Locate and identify every blood parasite.
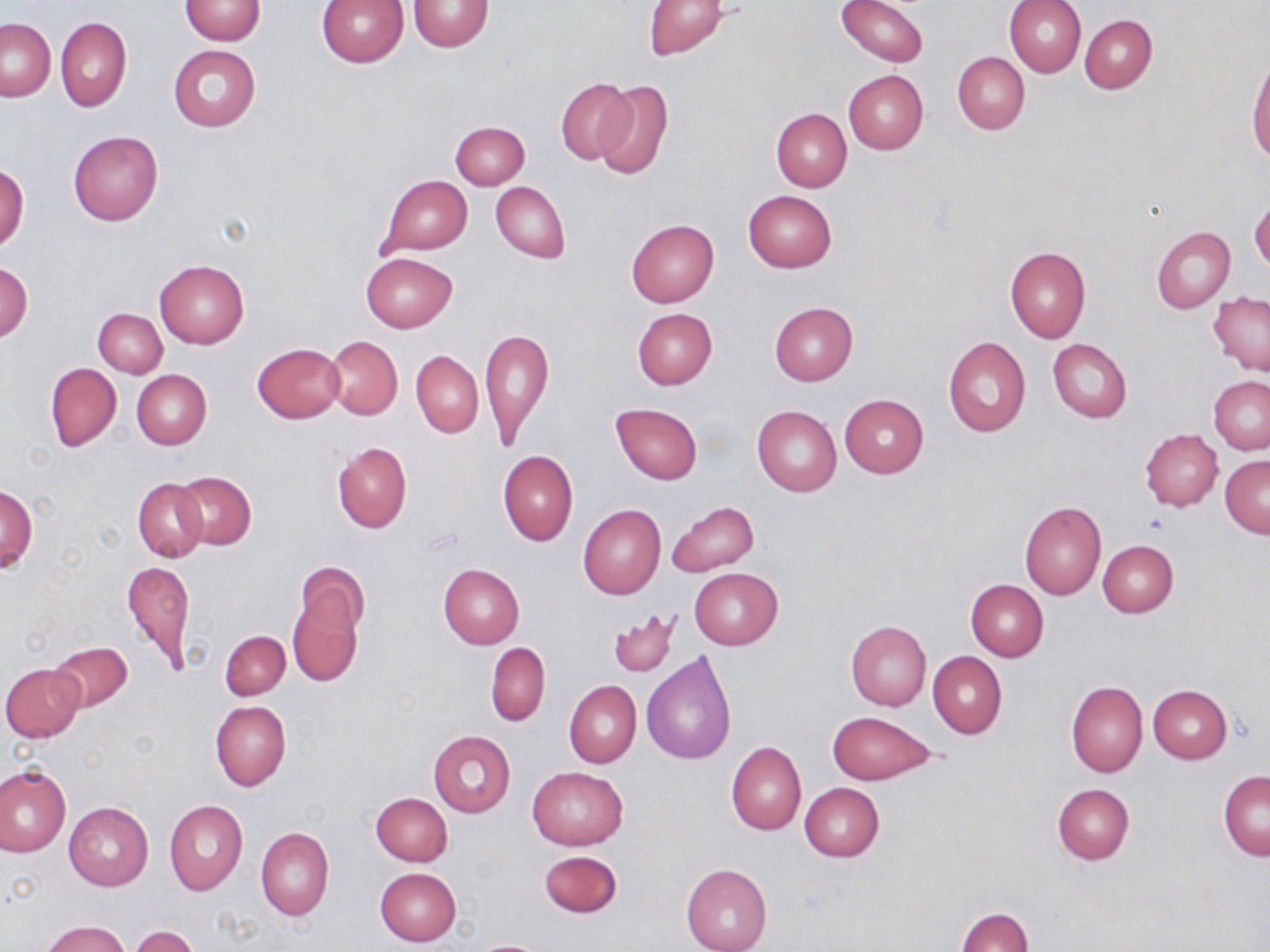
No blood parasites observed.

slide-level diagnosis = no evidence of blood parasites
uninfected red blood cell locations = approximate bounding boxes as named x1/y1/x2/y2 corners in pixels: (x1=181, y1=0, x2=266, y2=44), (x1=317, y1=0, x2=409, y2=68), (x1=837, y1=0, x2=927, y2=66), (x1=1005, y1=0, x2=1085, y2=77), (x1=409, y1=1, x2=493, y2=52), (x1=643, y1=1, x2=729, y2=60), (x1=1080, y1=14, x2=1156, y2=93), (x1=55, y1=17, x2=131, y2=113), (x1=1, y1=19, x2=55, y2=101), (x1=168, y1=44, x2=261, y2=132), (x1=952, y1=52, x2=1029, y2=135), (x1=1247, y1=53, x2=1270, y2=163), (x1=844, y1=71, x2=928, y2=155), (x1=555, y1=78, x2=637, y2=165), (x1=594, y1=81, x2=672, y2=179), (x1=771, y1=109, x2=851, y2=191), (x1=451, y1=121, x2=529, y2=188), (x1=67, y1=130, x2=163, y2=226), (x1=0, y1=164, x2=29, y2=252), (x1=379, y1=175, x2=472, y2=255), (x1=490, y1=181, x2=570, y2=263), (x1=744, y1=190, x2=836, y2=273), (x1=1249, y1=199, x2=1270, y2=271), (x1=626, y1=218, x2=718, y2=308), (x1=1152, y1=226, x2=1236, y2=313), (x1=1005, y1=247, x2=1090, y2=343), (x1=361, y1=252, x2=457, y2=333), (x1=154, y1=260, x2=248, y2=348), (x1=0, y1=262, x2=32, y2=344), (x1=1208, y1=292, x2=1270, y2=377), (x1=769, y1=303, x2=858, y2=386), (x1=93, y1=308, x2=168, y2=378), (x1=632, y1=308, x2=717, y2=390), (x1=480, y1=326, x2=552, y2=447), (x1=943, y1=335, x2=1030, y2=437), (x1=324, y1=336, x2=403, y2=420), (x1=1048, y1=339, x2=1132, y2=422), (x1=252, y1=343, x2=345, y2=422), (x1=411, y1=352, x2=483, y2=437), (x1=46, y1=363, x2=121, y2=452), (x1=131, y1=370, x2=210, y2=449), (x1=1209, y1=378, x2=1270, y2=454), (x1=839, y1=394, x2=928, y2=477), (x1=610, y1=403, x2=701, y2=485), (x1=752, y1=405, x2=841, y2=496), (x1=1140, y1=429, x2=1222, y2=512), (x1=332, y1=441, x2=412, y2=533), (x1=498, y1=450, x2=577, y2=546), (x1=1220, y1=455, x2=1270, y2=539), (x1=175, y1=472, x2=256, y2=549), (x1=133, y1=478, x2=208, y2=562), (x1=1, y1=484, x2=37, y2=573), (x1=667, y1=501, x2=760, y2=576), (x1=1019, y1=502, x2=1107, y2=600), (x1=578, y1=504, x2=666, y2=600), (x1=1098, y1=538, x2=1178, y2=618), (x1=124, y1=558, x2=194, y2=676), (x1=285, y1=564, x2=367, y2=694), (x1=438, y1=564, x2=523, y2=650), (x1=688, y1=567, x2=782, y2=650), (x1=965, y1=580, x2=1048, y2=663), (x1=609, y1=610, x2=679, y2=678), (x1=845, y1=622, x2=931, y2=708), (x1=220, y1=631, x2=290, y2=699), (x1=49, y1=641, x2=133, y2=714), (x1=486, y1=642, x2=550, y2=727), (x1=927, y1=651, x2=1006, y2=738), (x1=642, y1=653, x2=736, y2=765), (x1=1, y1=663, x2=84, y2=742), (x1=564, y1=681, x2=641, y2=769), (x1=1066, y1=681, x2=1147, y2=777), (x1=1148, y1=685, x2=1231, y2=763), (x1=210, y1=701, x2=291, y2=792), (x1=827, y1=711, x2=936, y2=785), (x1=428, y1=730, x2=516, y2=817), (x1=726, y1=741, x2=806, y2=835), (x1=0, y1=765, x2=70, y2=858), (x1=526, y1=768, x2=628, y2=850), (x1=1218, y1=771, x2=1269, y2=862), (x1=799, y1=782, x2=885, y2=862), (x1=1052, y1=783, x2=1134, y2=865), (x1=371, y1=793, x2=452, y2=866), (x1=164, y1=800, x2=248, y2=896), (x1=63, y1=802, x2=152, y2=890), (x1=256, y1=827, x2=334, y2=921), (x1=539, y1=851, x2=622, y2=917), (x1=681, y1=863, x2=772, y2=952), (x1=374, y1=867, x2=460, y2=947), (x1=955, y1=907, x2=1033, y2=952), (x1=41, y1=920, x2=131, y2=952), (x1=129, y1=926, x2=198, y2=952), (x1=469, y1=939, x2=551, y2=951)
magnification = 1000x
field of view = single
stain = May-Grünwald-Giemsa
modality = optical microscopy
preparation = thin blood film
image size = 1270×952 pixels